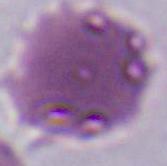
Summary:
  - Identification: red blood cell
  - Magnification: 1000x
  - Modality: micrograph